Give the position of every P. falciparum parasite, noting its life-cycle stage.
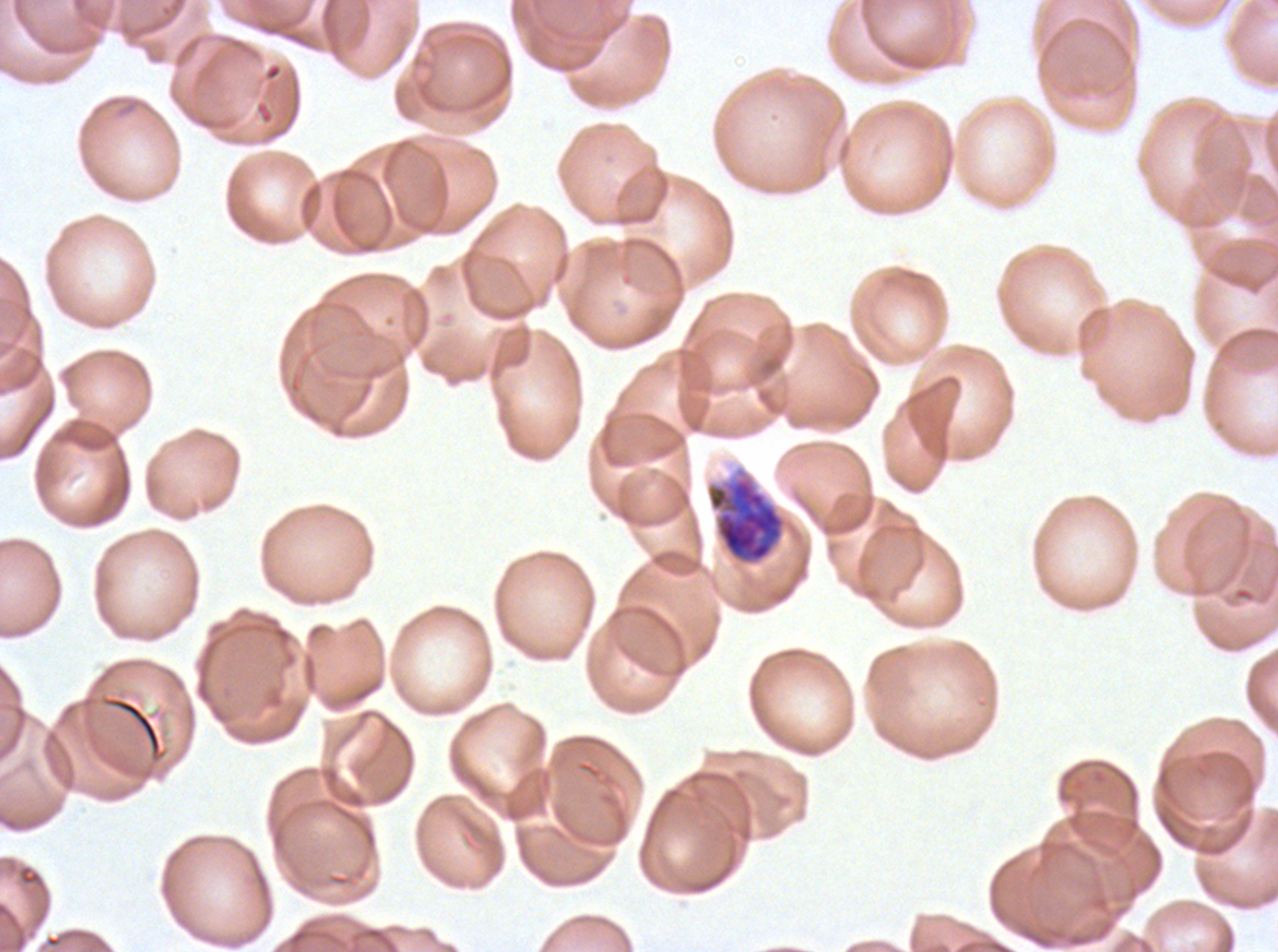

Approximate bounding boxes as (x1, y1, x2, y2) in pixels.
Early schizonts: (704, 465, 789, 568).
No rings, late-ring/early-trophozoite forms, mid trophozoites, late trophozoites, late schizonts, segmenters, or gametocytes observed.

Image is 1278×952 pixels. One sub-image of a larger composite. P. falciparum cultured ex vivo for 24 to 48 hours, from a patient in The Gambia. Thin blood film. Giemsa stain.